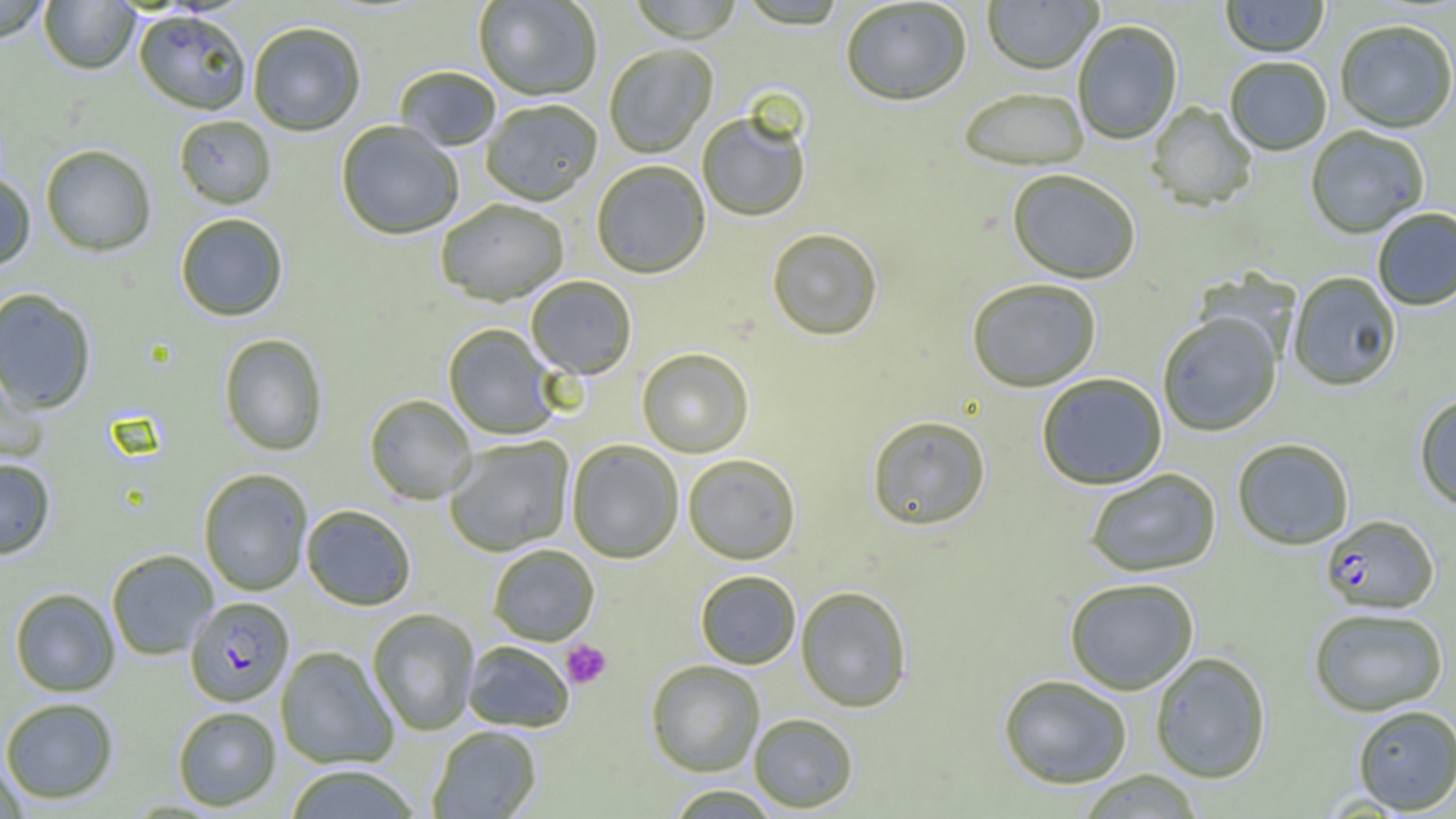

Approximate bounding boxes as (x1, y1, x2, y2) in pixels. Plasmodium falciparum-infected red blood cell locations: (1320, 516, 1439, 615), (185, 596, 293, 706). Platelet locations: (560, 640, 612, 689). Uninfected red blood cell locations: (0, 0, 52, 43), (473, 0, 603, 102), (628, 0, 744, 44), (982, 0, 1102, 77), (1220, 0, 1330, 59), (39, 1, 140, 75), (840, 1, 972, 108), (735, 2, 850, 32), (134, 10, 251, 116), (1073, 22, 1183, 145), (1335, 22, 1456, 135), (248, 23, 365, 137), (605, 46, 717, 159), (1224, 59, 1332, 157), (395, 67, 501, 152), (959, 90, 1090, 172), (481, 101, 603, 207), (1147, 102, 1257, 212), (697, 113, 810, 223), (174, 115, 277, 210), (336, 122, 464, 241), (1305, 127, 1430, 240), (40, 145, 156, 257), (591, 161, 710, 279), (1007, 171, 1140, 285), (0, 173, 36, 271), (435, 200, 569, 307), (1373, 209, 1456, 311), (175, 214, 288, 322), (766, 229, 883, 342), (1288, 272, 1401, 392), (526, 276, 637, 380), (967, 279, 1101, 393), (0, 288, 98, 414), (1158, 314, 1281, 437), (443, 324, 560, 440), (218, 334, 328, 456), (637, 349, 754, 458), (0, 365, 47, 466), (1037, 373, 1167, 491), (364, 394, 477, 504), (1414, 395, 1456, 512), (866, 416, 991, 532), (443, 436, 574, 557), (1232, 439, 1353, 550), (567, 440, 683, 563), (683, 455, 801, 565), (0, 459, 56, 559), (198, 468, 313, 596), (1085, 469, 1221, 578), (301, 505, 417, 611), (488, 544, 599, 646), (106, 549, 218, 660), (695, 570, 801, 669), (1064, 579, 1199, 695), (795, 586, 912, 713), (10, 588, 120, 697), (367, 608, 480, 736), (1309, 609, 1448, 717), (462, 641, 575, 733), (276, 646, 398, 769), (1150, 652, 1271, 784), (646, 660, 765, 777), (998, 674, 1132, 790), (0, 697, 119, 804), (1352, 705, 1456, 814), (173, 706, 281, 811), (749, 714, 859, 813), (427, 726, 542, 818), (0, 759, 29, 819), (283, 764, 422, 819), (1077, 771, 1205, 818), (665, 785, 782, 818). Slide-level diagnosis: Plasmodium falciparum. One field of a larger specimen. Thin blood film. Optical microscopy. Image is 1456×819 pixels. Captured at 1000x magnification.